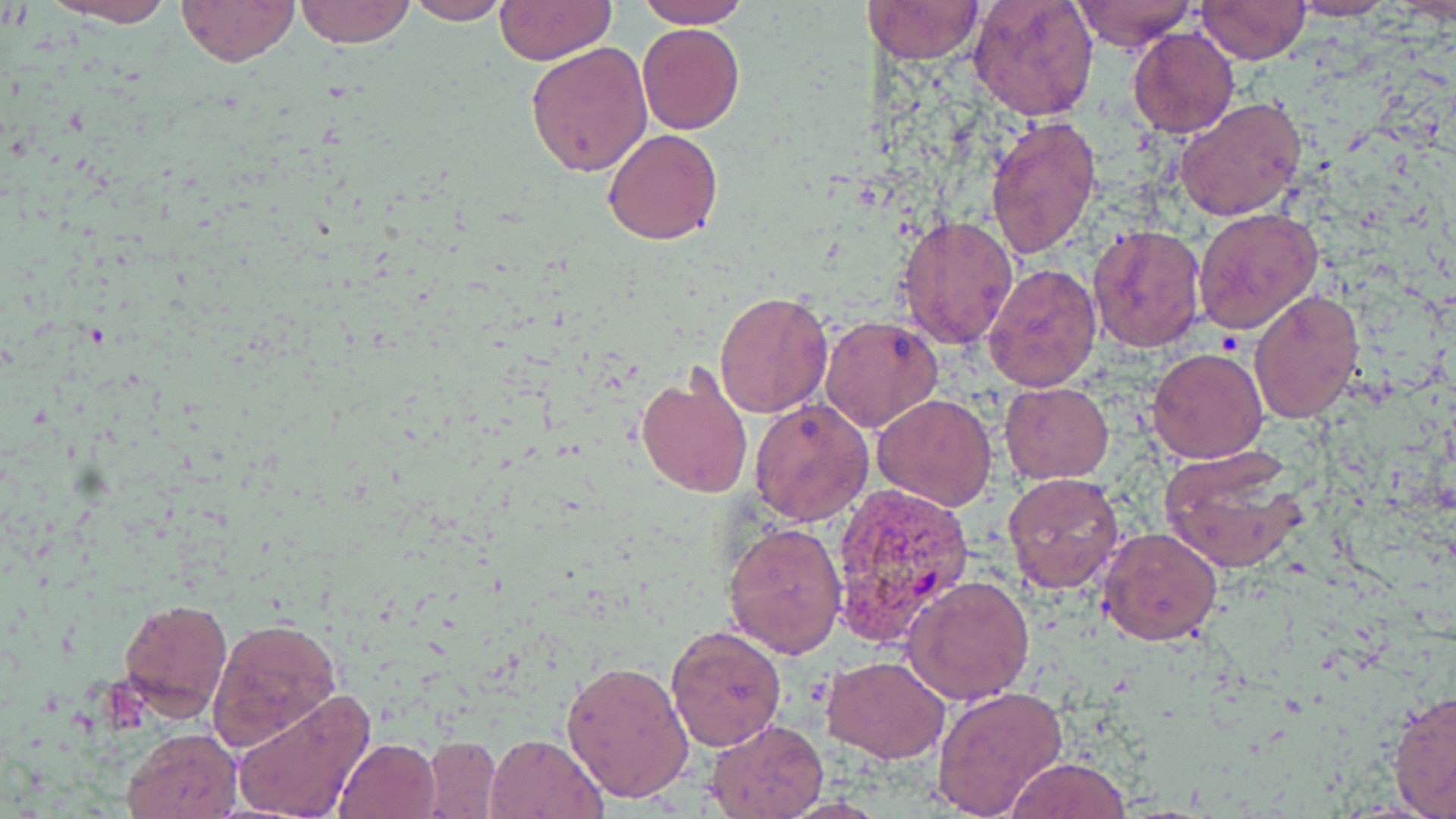 Approximate bounding boxes as (x1, y1, x2, y2) in pixels. Uninfected red blood cell locations: (38, 0, 180, 27), (177, 0, 298, 67), (294, 0, 416, 48), (969, 0, 1100, 122), (1072, 0, 1195, 53), (1290, 0, 1393, 20), (401, 1, 517, 24), (494, 1, 617, 66), (637, 1, 752, 28), (1196, 1, 1311, 62), (867, 2, 985, 63), (636, 24, 744, 135), (1127, 27, 1239, 137), (527, 41, 655, 178), (1174, 96, 1308, 223), (985, 116, 1102, 258), (603, 127, 724, 245), (1193, 206, 1323, 334), (897, 213, 1019, 349), (1088, 224, 1208, 354), (984, 262, 1101, 394), (1248, 289, 1366, 424), (714, 290, 833, 418), (820, 315, 944, 434), (1171, 319, 1352, 451), (1146, 347, 1269, 463), (636, 368, 754, 499), (1000, 381, 1113, 483), (871, 393, 998, 511), (750, 399, 874, 525), (1159, 448, 1308, 573), (1004, 474, 1125, 592), (723, 521, 848, 659), (1096, 526, 1222, 646), (904, 573, 1037, 705), (118, 597, 233, 719), (208, 617, 341, 748), (665, 624, 786, 752), (821, 655, 948, 762), (561, 657, 695, 804), (932, 684, 1071, 817), (230, 689, 376, 819), (1386, 689, 1456, 817), (706, 718, 828, 819), (122, 728, 243, 819), (485, 732, 610, 819), (422, 736, 502, 819), (334, 737, 440, 819), (1005, 757, 1132, 818). Plasmodium vivax-infected red blood cell locations: (830, 485, 972, 646). Slide-level diagnosis: Plasmodium vivax. Single field of view. May-Grünwald-Giemsa stain. Light microscopy. Image is 1456×819 pixels. Thin blood film. 1000x magnification.